State which parasite is depicted.
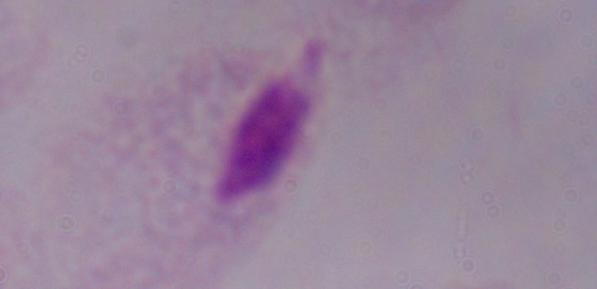

A trichomonad.

Micrograph. Captured at 1000x magnification.